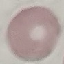
result = no malaria parasites detected
preparation = thin smear
capture = smartphone camera at the microscope eyepiece
image type = automatically extracted cell patch, resized to 64 × 64 pixels
stain = Giemsa